Report the malaria status of this cell.
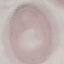
Uninfected.

capture = smartphone through the microscope eyepiece
stain = Giemsa
image type = cell patch, automatically extracted from a larger field of view and resized to 64 × 64 pixels
preparation = thin smear